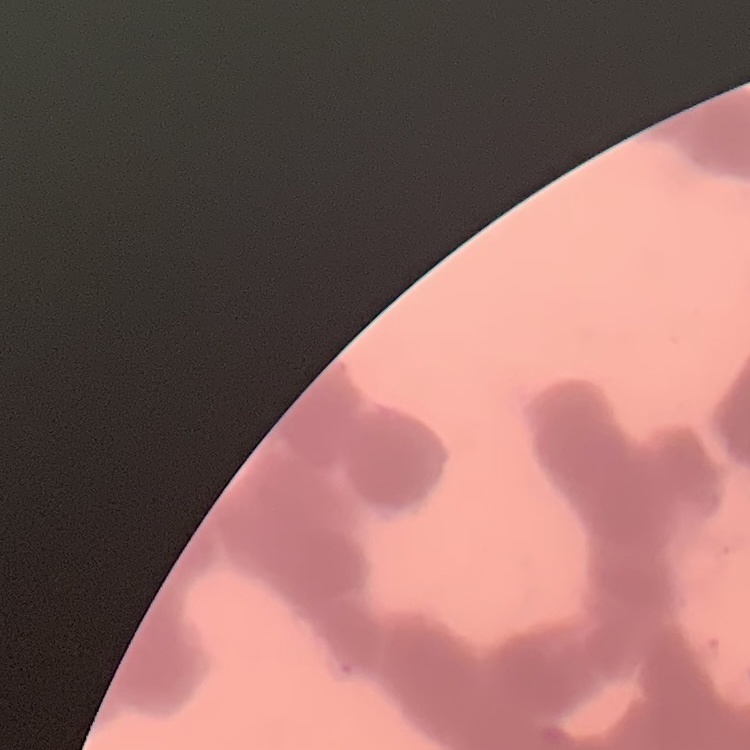
erythrocyte morphology = rouleaux formation
image type = one tile cut from a larger photomicrograph
stain = Field's or Giemsa
preparation = thin peripheral smear